Identify the blood parasite species.
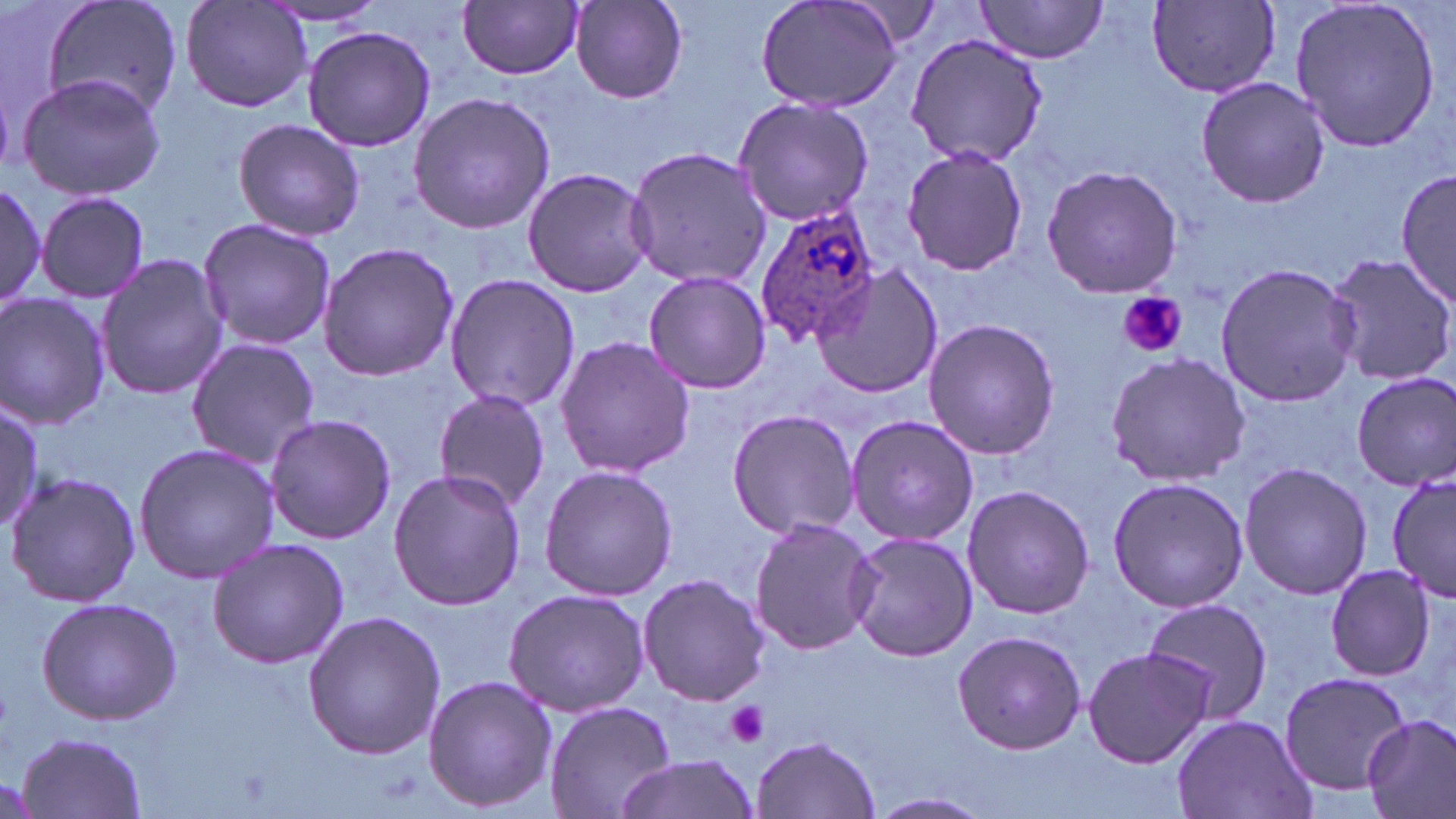
Plasmodium ovale.

platelet locations = approximate bounding boxes as (x1, y1, x2, y2) in pixels: (1116, 293, 1187, 358), (726, 701, 770, 747)
magnification = 1000x
modality = optical microscopy
Plasmodium ovale-infected red blood cell locations = approximate bounding boxes as (x1, y1, x2, y2) in pixels: (754, 204, 879, 347)
preparation = thin blood film
uninfected red blood cell locations = approximate bounding boxes as (x1, y1, x2, y2) in pixels: (40, 0, 185, 125), (178, 0, 312, 115), (754, 0, 901, 114), (970, 0, 1110, 63), (1288, 0, 1443, 152), (1148, 1, 1281, 95), (255, 2, 394, 26), (460, 2, 584, 79), (569, 2, 688, 103), (302, 26, 437, 154), (906, 31, 1048, 168), (16, 72, 167, 202), (1193, 76, 1331, 209), (407, 92, 556, 234), (734, 96, 877, 227), (232, 118, 366, 242), (901, 144, 1028, 278), (623, 147, 774, 290), (1040, 164, 1184, 299), (1395, 165, 1454, 308), (520, 167, 657, 298), (0, 176, 50, 312), (36, 191, 150, 304), (196, 218, 336, 352), (317, 241, 458, 382), (1321, 251, 1456, 389), (95, 253, 230, 401), (1213, 262, 1360, 409), (812, 266, 946, 400), (643, 270, 772, 393), (444, 274, 581, 413), (0, 292, 112, 431), (921, 318, 1061, 460), (553, 335, 698, 478), (183, 336, 319, 475), (1103, 350, 1251, 487), (1351, 371, 1456, 492), (430, 390, 554, 513), (0, 405, 45, 530), (725, 407, 861, 539), (264, 415, 397, 544), (846, 416, 980, 545), (132, 441, 282, 584), (1238, 459, 1372, 600), (538, 464, 677, 601), (388, 468, 526, 612), (1386, 468, 1455, 606), (5, 470, 143, 609), (1106, 476, 1250, 613), (960, 484, 1097, 619), (748, 517, 882, 655), (845, 531, 979, 662), (206, 535, 353, 668), (1323, 564, 1439, 681), (636, 573, 770, 706), (503, 586, 649, 718), (35, 597, 184, 725), (1141, 599, 1276, 725), (301, 609, 446, 762), (950, 629, 1087, 754), (1082, 645, 1210, 769), (1275, 670, 1411, 793), (422, 675, 557, 813), (545, 700, 674, 819), (1170, 713, 1317, 819), (1362, 714, 1456, 819), (14, 731, 148, 818), (753, 734, 880, 818), (609, 754, 756, 819), (866, 791, 995, 819)
stain = May-Grünwald-Giemsa
field of view = one of a larger specimen
image size = 1456×819 pixels